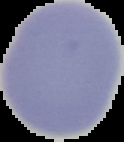
Summary:
  - Image size: 124×142 pixels
  - Malaria status: uninfected
  - Preparation: thin blood film
  - Image type: cell region segmented out of the field of view; surrounding area masked to black